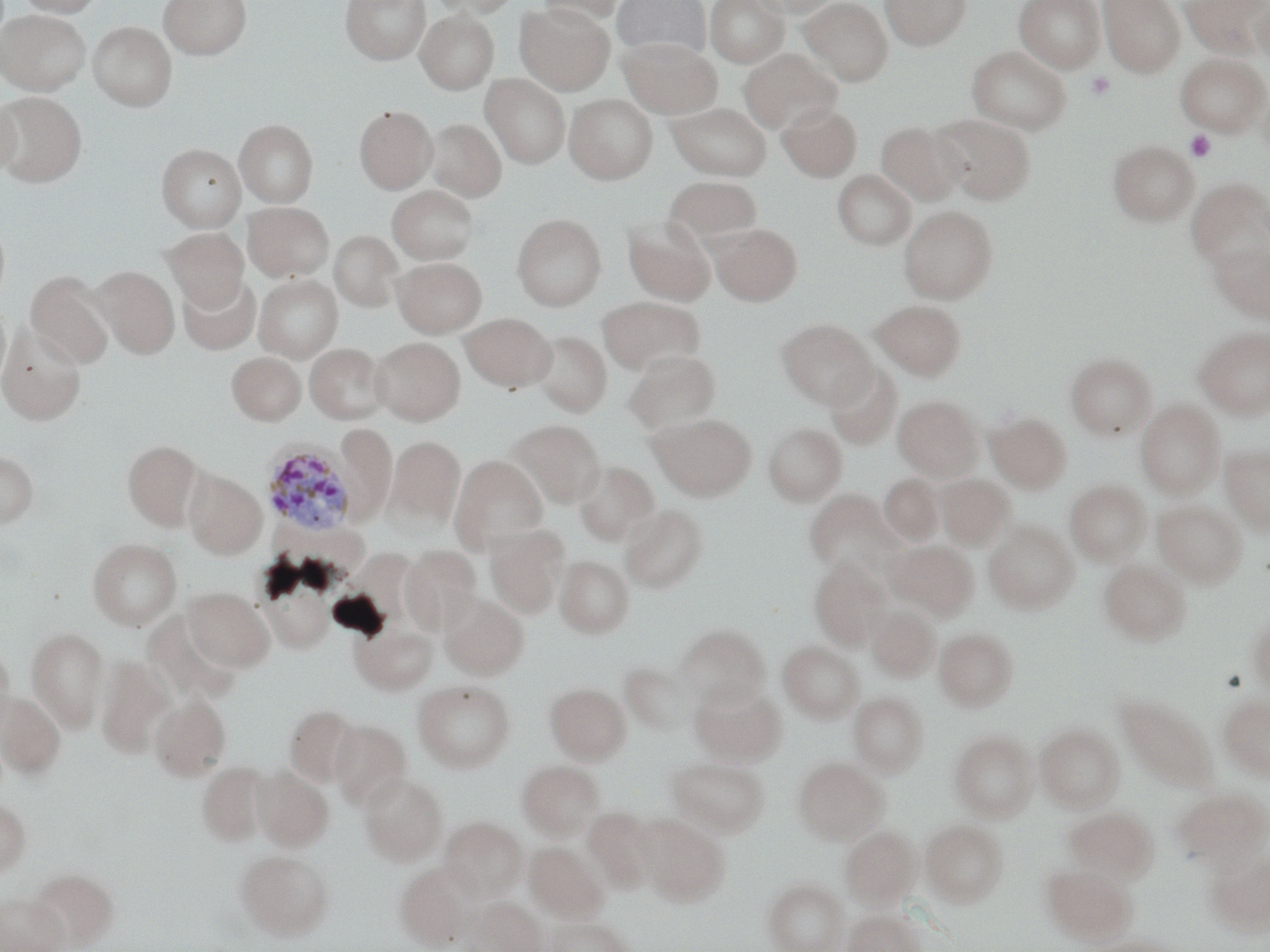 Approximate bounding boxes as (x1, y1, x2, y2) in pixels. Uninfected red blood cell locations: (15, 0, 105, 16), (159, 0, 251, 59), (340, 0, 429, 64), (426, 0, 521, 19), (533, 0, 629, 25), (612, 0, 712, 60), (705, 0, 789, 67), (748, 0, 841, 19), (799, 0, 893, 85), (880, 0, 972, 50), (1014, 0, 1106, 73), (1098, 0, 1185, 77), (1180, 0, 1267, 55), (1248, 1, 1270, 68), (515, 4, 614, 94), (0, 9, 90, 95), (415, 9, 499, 94), (87, 21, 177, 111), (620, 37, 721, 118), (967, 45, 1072, 134), (739, 49, 840, 133), (1175, 52, 1269, 135), (481, 73, 570, 169), (0, 93, 87, 187), (0, 93, 20, 179), (564, 94, 657, 183), (666, 102, 772, 180), (777, 103, 862, 181), (354, 105, 437, 193), (932, 113, 1035, 203), (426, 118, 506, 201), (234, 119, 318, 207), (876, 121, 967, 205), (1107, 140, 1199, 225), (156, 143, 246, 232), (833, 169, 916, 249), (663, 176, 762, 249), (1186, 178, 1270, 270), (387, 185, 479, 264), (243, 202, 334, 282), (898, 205, 998, 304), (0, 212, 11, 314), (511, 213, 606, 310), (622, 218, 716, 305), (710, 223, 802, 305), (164, 228, 249, 310), (330, 230, 403, 311), (1208, 238, 1270, 320), (393, 257, 487, 337), (90, 265, 179, 358), (25, 269, 115, 368), (178, 273, 262, 355), (254, 275, 342, 362), (598, 296, 704, 374), (871, 300, 966, 381), (0, 301, 11, 394), (461, 312, 556, 392), (777, 319, 876, 407), (0, 324, 86, 425), (1194, 326, 1270, 419), (529, 331, 611, 416), (370, 337, 465, 425), (305, 343, 390, 425), (624, 350, 720, 432), (226, 351, 306, 425), (1066, 353, 1156, 439), (824, 363, 902, 450), (893, 395, 983, 481), (1135, 399, 1225, 497), (986, 411, 1072, 493), (648, 413, 756, 500), (509, 419, 605, 508), (763, 423, 847, 505), (334, 424, 396, 526), (385, 435, 465, 531), (122, 439, 204, 529), (1220, 445, 1270, 534), (0, 450, 38, 527), (449, 454, 548, 553), (572, 460, 659, 546), (183, 468, 267, 559), (879, 474, 943, 545), (936, 474, 1014, 549), (1065, 479, 1151, 565), (804, 490, 900, 577), (1153, 500, 1247, 588), (621, 504, 707, 593), (984, 522, 1078, 613), (484, 524, 570, 618), (88, 538, 181, 630), (886, 540, 978, 620), (400, 546, 481, 631), (554, 555, 634, 638), (808, 556, 893, 649), (1099, 560, 1191, 646), (257, 563, 336, 654), (183, 586, 275, 672), (439, 592, 528, 680), (865, 605, 940, 682), (143, 611, 240, 706), (1248, 616, 1270, 692), (672, 624, 769, 709), (350, 625, 437, 695), (26, 626, 109, 733), (934, 627, 1019, 711), (0, 641, 15, 741), (778, 641, 864, 723), (95, 655, 172, 759), (622, 664, 693, 735), (690, 679, 787, 766), (413, 680, 514, 772), (545, 683, 631, 764), (0, 690, 66, 777), (848, 691, 929, 777), (150, 695, 231, 781), (1116, 695, 1219, 792), (1218, 695, 1270, 780), (284, 703, 361, 787), (330, 719, 411, 812), (1036, 723, 1125, 812), (949, 730, 1039, 822), (667, 756, 770, 837), (792, 757, 887, 844), (517, 760, 604, 839), (196, 761, 272, 846), (252, 766, 333, 851), (359, 772, 448, 865), (1171, 787, 1270, 870), (0, 796, 31, 882), (1064, 806, 1157, 883), (584, 807, 656, 892), (637, 814, 729, 906), (439, 816, 529, 902), (921, 819, 1008, 907), (840, 825, 921, 908), (525, 842, 609, 923), (1203, 847, 1270, 937), (234, 849, 334, 940), (395, 863, 477, 950), (1043, 863, 1136, 944), (28, 867, 120, 951), (764, 879, 848, 952), (0, 891, 68, 952), (463, 896, 547, 952), (843, 908, 925, 952), (543, 915, 633, 951), (1090, 936, 1179, 952). Plasmodium ovale-infected red blood cell locations: (261, 441, 357, 537). Platelet locations: (1085, 71, 1116, 100), (1185, 129, 1217, 163). Slide-level diagnosis: Plasmodium ovale. Light microscopy. 1000x magnification. Image is 1270×952 pixels. Thin blood film. One field of a larger specimen. May-Grünwald-Giemsa stain.